Assess this cell for malaria.
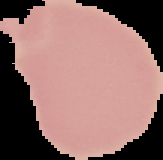

Uninfected.

Segmented cell region on a black background. Image is 163×160 pixels. From a thin blood film.